Identify the preparation type.
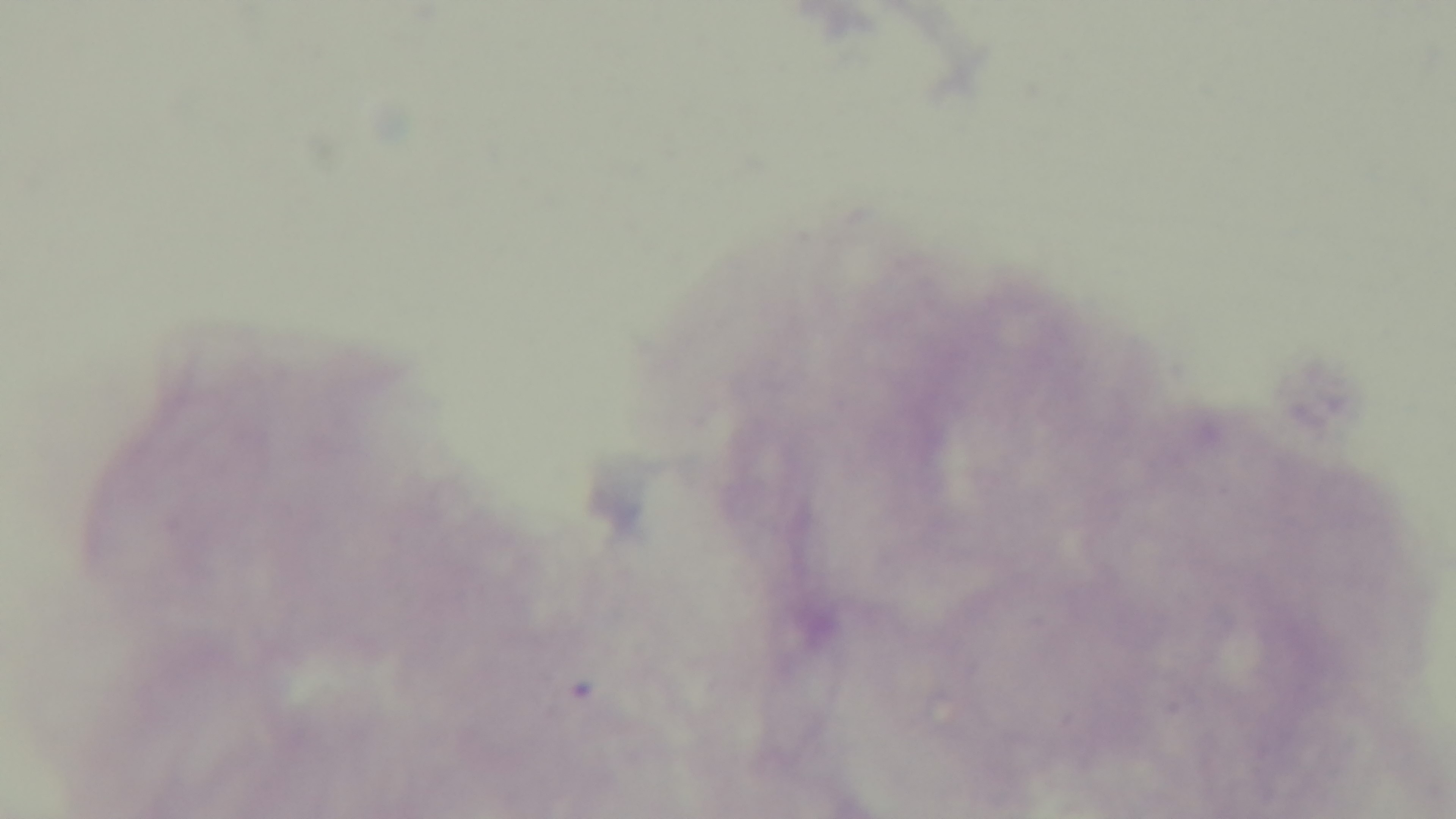

A thick smear.

Giemsa-stained. One field from the slide. Oil-immersion objective, 100x. Malaria status: uninfected. Light microscopy. Captured with a mounted 4K digital camera.